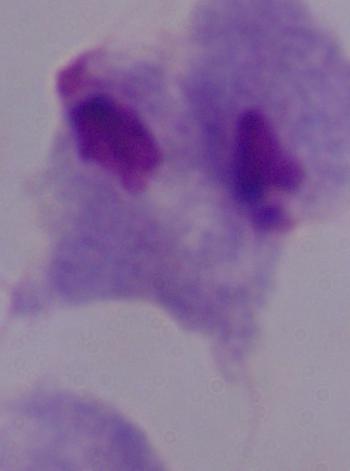 Micrograph. A trichomonad is seen. Captured at 1000x magnification.